Describe the morphology of the erythrocytes.
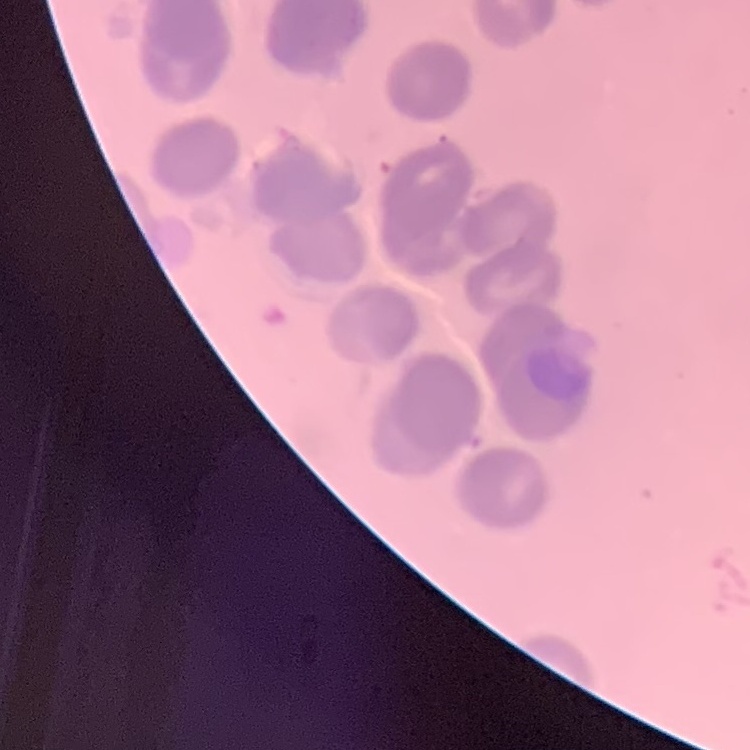
Rouleaux formation.

stain = Field's or Giemsa
image type = square crop of a larger photomicrograph
preparation = thin peripheral smear